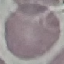
Summary:
  - Malaria status: uninfected
  - Image type: automatically extracted cell patch, resized to 64 × 64 pixels
  - Stain: Giemsa
  - Capture: smartphone camera at the microscope eyepiece
  - Preparation: thin smear